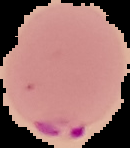

preparation: thin blood film
result: Plasmodium parasites detected
image_type: cell region segmented out of the field of view; surrounding area masked to black
image_size: 130×148 pixels